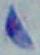

Summary:
  - Identification: Toxoplasma gondii
  - Modality: micrograph
  - Magnification: 1000x